Comment on the morphology of the erythrocytes.
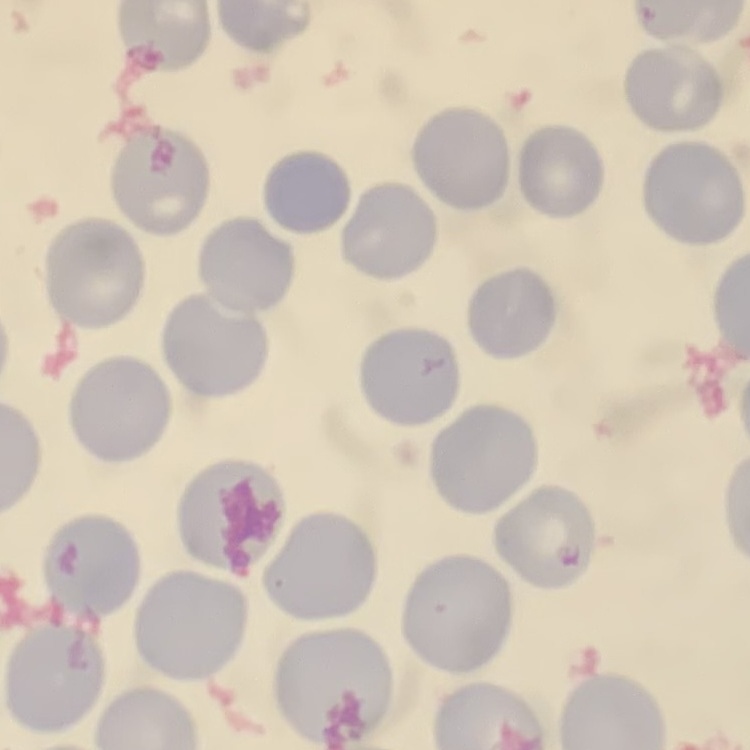

They show no rouleaux formation.

Thin peripheral smear. Square crop of a larger photomicrograph. Field's or Giemsa stain.